Outline every parasitised red blood cell, every trophozoite, every gametocyte, every leukocyte, and every artifact (platelet-like body, stain precipitate, or debris).
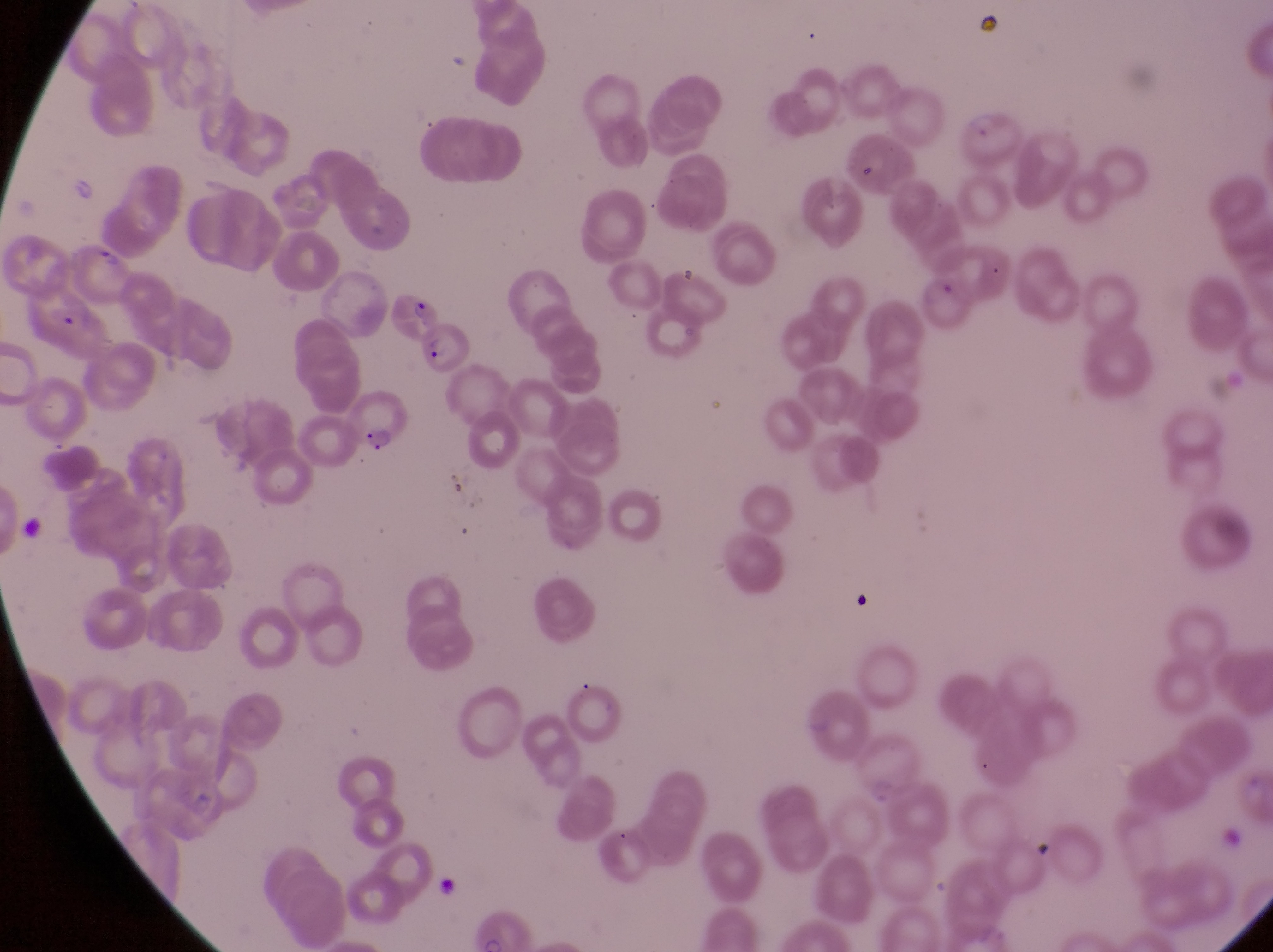
Approximate bounding boxes as (left, top, right, bottom) in pixels.
Parasitised red blood cells: (74, 242, 141, 307), (385, 285, 443, 343), (20, 292, 110, 359), (424, 322, 479, 370), (342, 392, 405, 452).
No leukocytes observed.

preparation = thin blood smear
country = Uganda
image size = 1273×952 pixels
magnification = 1000x
field of view = single
capture = smartphone photograph through the eyepiece of an Olympus CX-23 microscope